Assess for malaria.
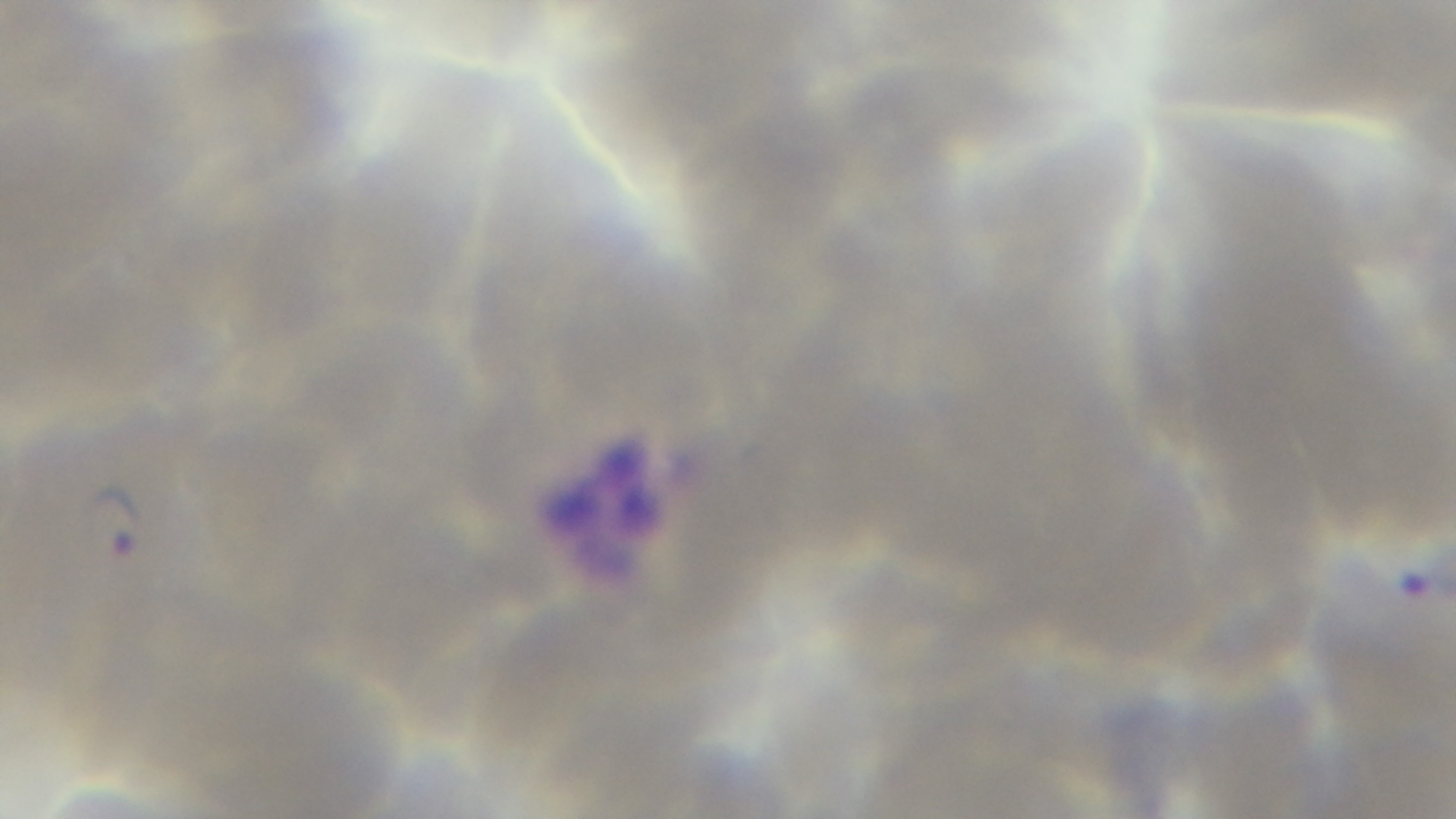
Infected.

Giemsa-stained. Preparation: thin blood film. Light microscopy. One field from the slide. Oil-immersion objective, 100x. Mounted 4K digital camera.